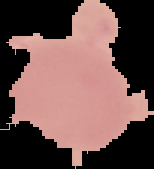

preparation: thin blood smear
image_size: 154×169 pixels
result: no Plasmodium parasites seen
image_type: segmented cell region on a black background